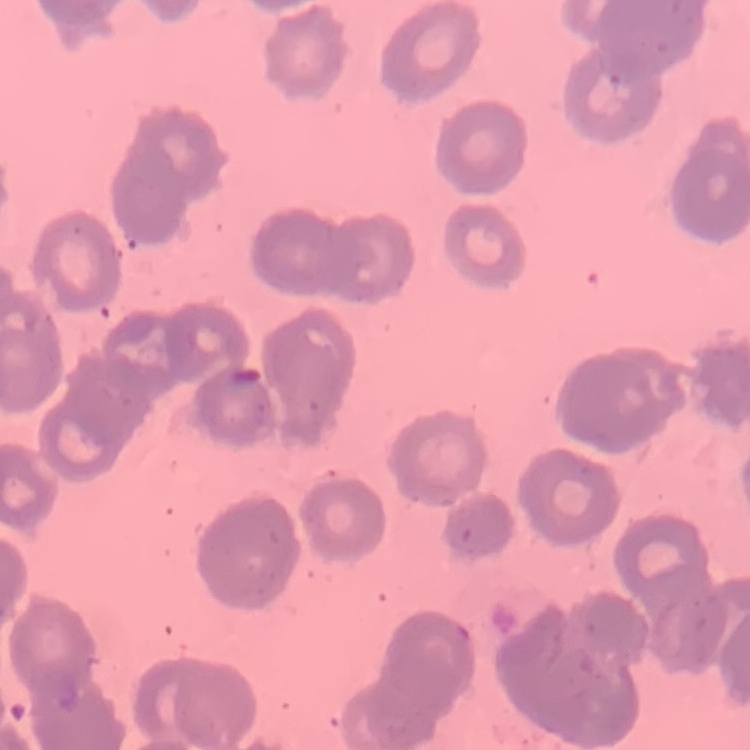
red_blood_cell_morphology: rouleaux formation
image_type: one tile cut from a larger photomicrograph
preparation: thin blood film
stain: Field's or Giemsa